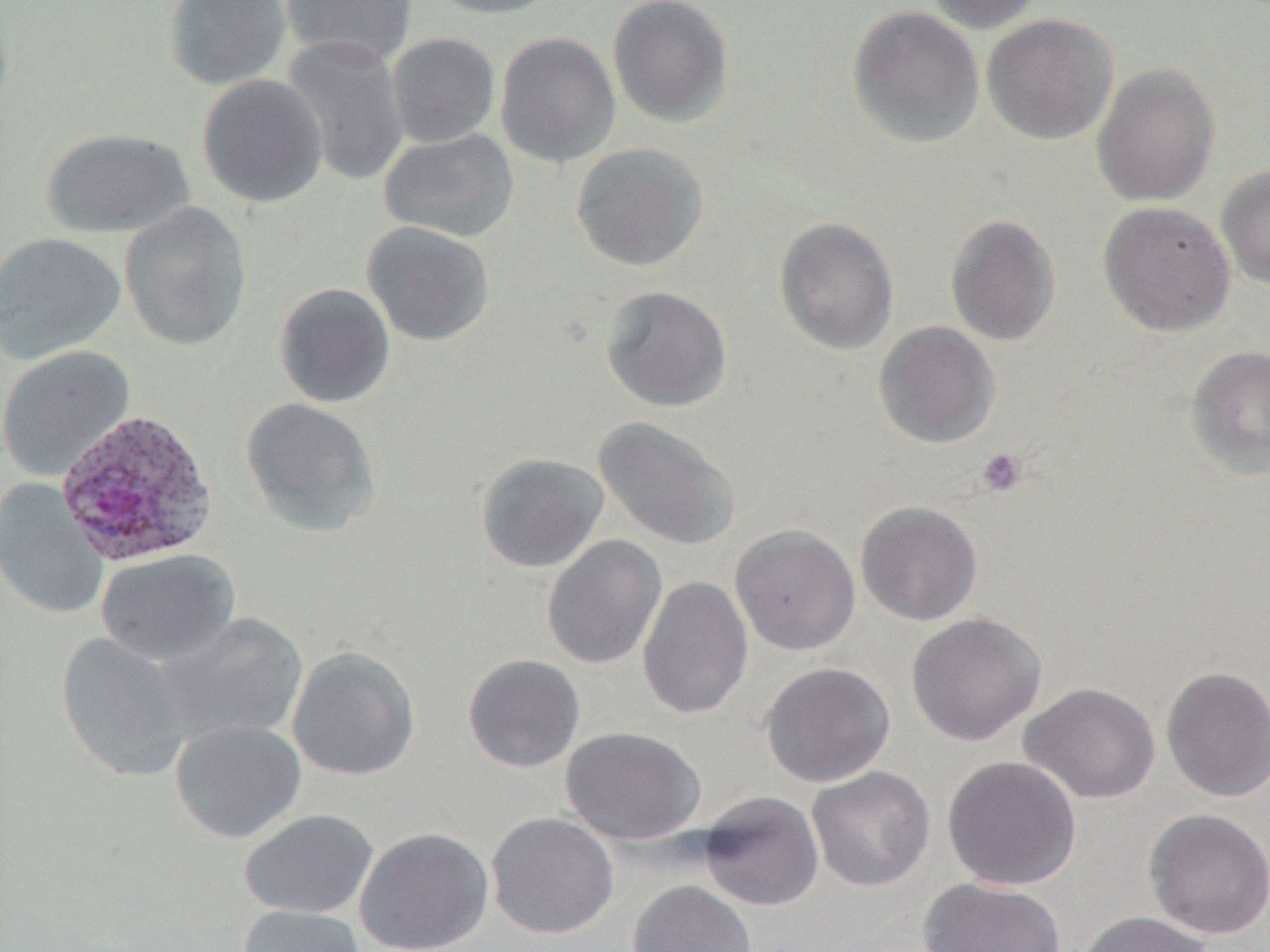

slide-level diagnosis = Plasmodium ovale
preparation = thin blood film
magnification = 1000x
Plasmodium ovale-infected red blood cell locations = approximate bounding boxes as [x1, y1, x2, y2] in pixels: [54, 407, 219, 566]
platelet locations = approximate bounding boxes as [x1, y1, x2, y2] in pixels: [975, 447, 1030, 498]
modality = light microscopy
field of view = single
image size = 1270×952 pixels
uninfected red blood cell locations = approximate bounding boxes as [x1, y1, x2, y2] in pixels: [163, 0, 292, 91], [281, 0, 417, 67], [423, 0, 567, 19], [608, 0, 734, 128], [923, 0, 1047, 33], [846, 6, 985, 150], [982, 13, 1118, 145], [495, 31, 621, 168], [386, 33, 500, 148], [282, 34, 409, 187], [1091, 62, 1220, 206], [197, 73, 328, 208], [42, 128, 196, 239], [379, 129, 519, 242], [571, 142, 709, 272], [1216, 165, 1270, 288], [118, 201, 253, 352], [1098, 201, 1235, 336], [944, 213, 1062, 347], [773, 217, 900, 355], [361, 221, 496, 346], [0, 232, 126, 365], [274, 282, 396, 408], [600, 285, 732, 412], [873, 321, 1000, 449], [0, 345, 135, 480], [1186, 345, 1270, 481], [241, 397, 382, 538], [592, 416, 741, 551], [475, 452, 609, 573], [0, 478, 109, 620], [855, 500, 984, 626], [730, 524, 861, 655], [541, 534, 667, 670], [95, 549, 240, 665], [637, 575, 753, 720], [155, 612, 309, 746], [906, 612, 1046, 746], [55, 632, 194, 781], [287, 645, 421, 781], [462, 653, 586, 773], [759, 661, 896, 788], [1161, 665, 1270, 803], [1019, 681, 1160, 804], [170, 719, 307, 842], [561, 726, 706, 845], [942, 755, 1081, 891], [806, 766, 935, 892], [697, 791, 825, 912], [1143, 807, 1270, 940], [239, 809, 379, 919], [486, 811, 620, 939], [354, 827, 495, 952], [918, 877, 1067, 952], [627, 881, 758, 952], [238, 905, 367, 952], [1073, 911, 1217, 952]